Classify this cell by malaria status.
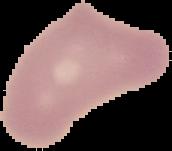

It is uninfected.

Summary:
  - Image type: segmented cell region on a black background
  - Preparation: thin blood film
  - Image size: 172×151 pixels